State the blood parasite species.
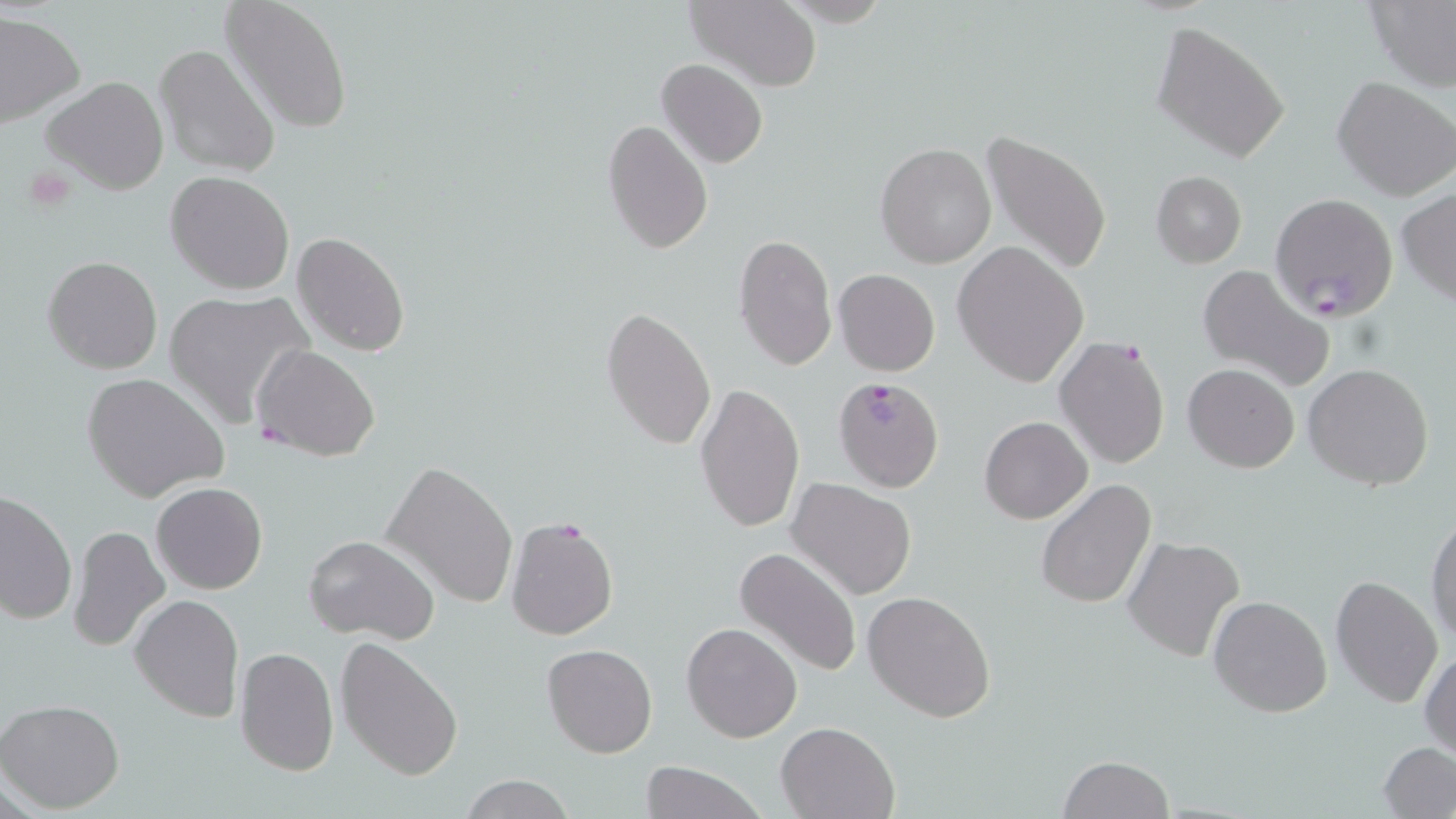
Plasmodium falciparum.

Summary:
  - Coordinate format: approximate bounding boxes as named x1/y1/x2/y2 corners in pixels
  - Plasmodium falciparum-infected red blood cell locations: (x1=1269, y1=194, x2=1398, y2=320), (x1=252, y1=344, x2=380, y2=462), (x1=833, y1=376, x2=945, y2=493)
  - Platelet locations: (x1=22, y1=166, x2=78, y2=213)
  - Uninfected red blood cell locations: (x1=219, y1=0, x2=354, y2=134), (x1=684, y1=0, x2=823, y2=91), (x1=1365, y1=0, x2=1456, y2=91), (x1=0, y1=12, x2=85, y2=127), (x1=1150, y1=22, x2=1291, y2=165), (x1=153, y1=44, x2=281, y2=180), (x1=657, y1=59, x2=768, y2=168), (x1=42, y1=76, x2=169, y2=195), (x1=1332, y1=76, x2=1456, y2=203), (x1=603, y1=116, x2=713, y2=257), (x1=980, y1=131, x2=1113, y2=278), (x1=877, y1=143, x2=997, y2=267), (x1=166, y1=171, x2=294, y2=295), (x1=1150, y1=171, x2=1246, y2=268), (x1=1397, y1=189, x2=1456, y2=306), (x1=291, y1=231, x2=411, y2=358), (x1=733, y1=233, x2=837, y2=369), (x1=952, y1=241, x2=1090, y2=387), (x1=43, y1=255, x2=163, y2=374), (x1=1196, y1=263, x2=1335, y2=392), (x1=834, y1=269, x2=940, y2=376), (x1=165, y1=288, x2=314, y2=429), (x1=602, y1=306, x2=716, y2=452), (x1=1054, y1=335, x2=1173, y2=471), (x1=1303, y1=362, x2=1435, y2=492), (x1=1183, y1=363, x2=1299, y2=473), (x1=83, y1=372, x2=229, y2=505), (x1=696, y1=381, x2=805, y2=532), (x1=978, y1=415, x2=1093, y2=524), (x1=381, y1=461, x2=518, y2=609), (x1=788, y1=477, x2=915, y2=599), (x1=1036, y1=478, x2=1157, y2=611), (x1=152, y1=482, x2=268, y2=595), (x1=0, y1=493, x2=75, y2=627), (x1=1426, y1=512, x2=1456, y2=646), (x1=504, y1=516, x2=618, y2=641), (x1=68, y1=525, x2=170, y2=652), (x1=305, y1=534, x2=440, y2=643), (x1=1123, y1=534, x2=1246, y2=663), (x1=734, y1=547, x2=864, y2=678), (x1=1330, y1=575, x2=1445, y2=709), (x1=864, y1=591, x2=995, y2=722), (x1=130, y1=594, x2=244, y2=724), (x1=1208, y1=595, x2=1331, y2=718), (x1=680, y1=622, x2=802, y2=743), (x1=335, y1=636, x2=464, y2=781), (x1=542, y1=643, x2=657, y2=757), (x1=234, y1=645, x2=339, y2=776), (x1=1420, y1=649, x2=1455, y2=760), (x1=0, y1=698, x2=126, y2=812), (x1=778, y1=722, x2=898, y2=819), (x1=1379, y1=741, x2=1456, y2=818), (x1=1058, y1=755, x2=1174, y2=818), (x1=641, y1=761, x2=767, y2=819), (x1=459, y1=774, x2=574, y2=819)
  - Stain: May-Grünwald-Giemsa
  - Modality: light microscopy
  - Preparation: thin blood film
  - Magnification: 1000x
  - Field of view: one of a larger specimen
  - Image size: 1456×819 pixels